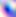

Summary:
  - Modality: photomicrograph
  - Magnification: 400x
  - Identification: Toxoplasma gondii